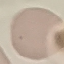

{
  "malaria_status": "uninfected",
  "preparation": "thin smear",
  "image_type": "cell patch, automatically extracted from a larger field of view and resized to 64 × 64 pixels",
  "capture": "smartphone camera at the microscope eyepiece",
  "stain": "Giemsa"
}